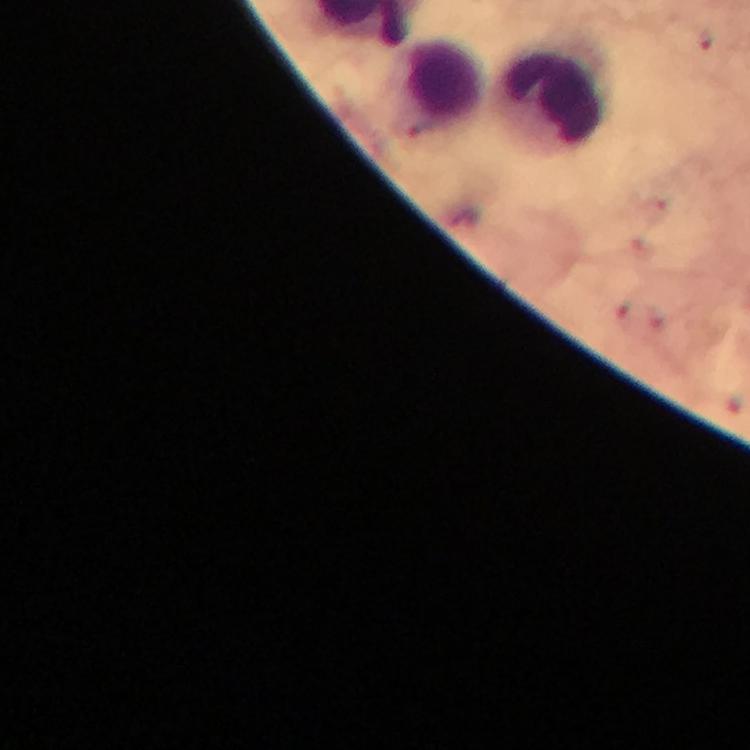

{
  "immersion_oil": "applied",
  "magnification": "100x",
  "cropped_from": "one field of view",
  "context": "from a malaria diagnostic workup",
  "malaria_parasite_locations": "approximate centers as {x, y} in pixels: {707, 37}",
  "preparation": "thick blood film",
  "leukocyte_locations": "approximate centers as {x, y} in pixels: {437, 87}, {547, 99}",
  "capture": "smartphone photograph through a microscope",
  "stain": "Giemsa",
  "image_size": "750×750 pixels"
}